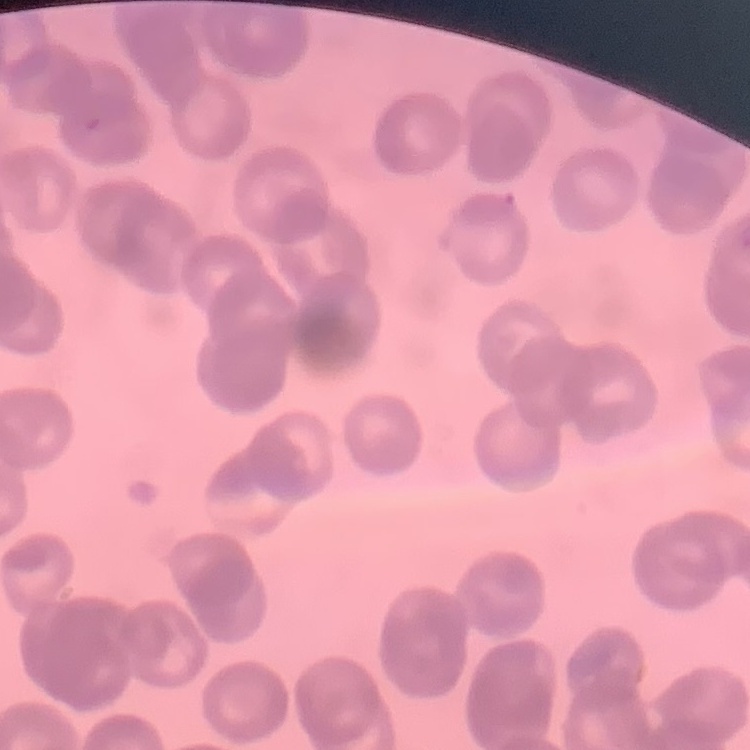
The red blood cells show rouleaux formation. Stained with either Field's or Giemsa. One tile cut from a larger photomicrograph. Thin blood smear.